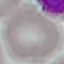
Summary:
  - Result: no malaria parasites seen
  - Image type: automatically extracted cell patch, resized to 64 × 64 pixels
  - Capture: smartphone through the microscope eyepiece
  - Stain: Giemsa
  - Preparation: thin blood film